Assess this cell for malaria.
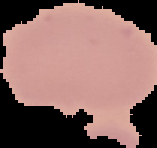

Uninfected.

Segmented cell region on a black background. From a thin blood film. Image is 157×148 pixels.